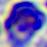

Photomicrograph. A white blood cell is shown. Captured at 400x magnification.